Give the position of every Plasmodium parasite visible.
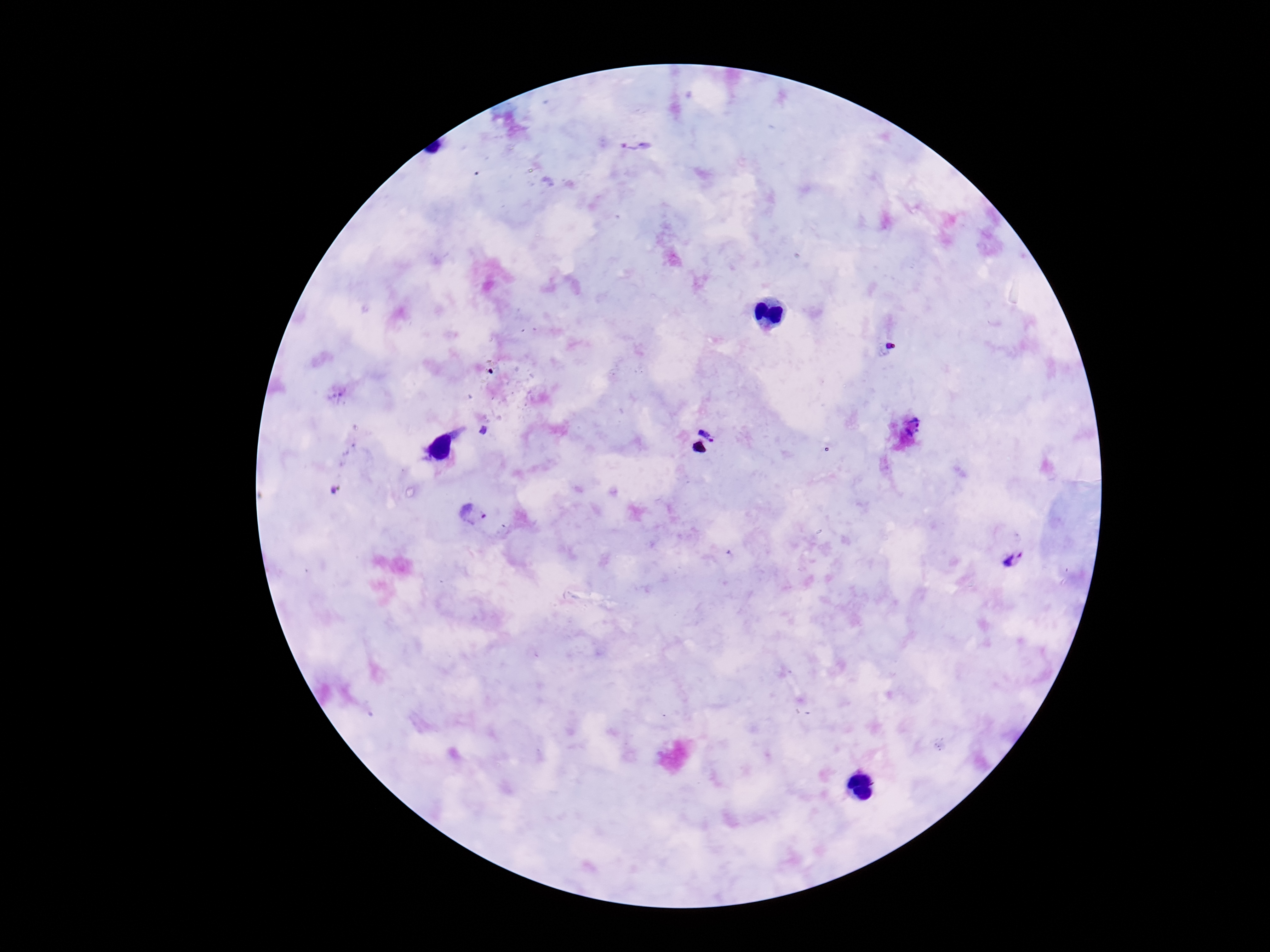
Approximate centers as (x, y) in pixels.
Plasmodium parasites: (635, 144), (712, 423), (913, 427), (474, 514), (1015, 560).

Summary:
  - Magnification: 100x
  - Stain: Giemsa
  - Preparation: thick peripheral-blood smear
  - Image size: 1270×952 pixels
  - Patient malaria status: infected
  - Field of view: one from this slide
  - Capture: smartphone camera through the microscope eyepiece